Comment on the morphology of the erythrocytes.
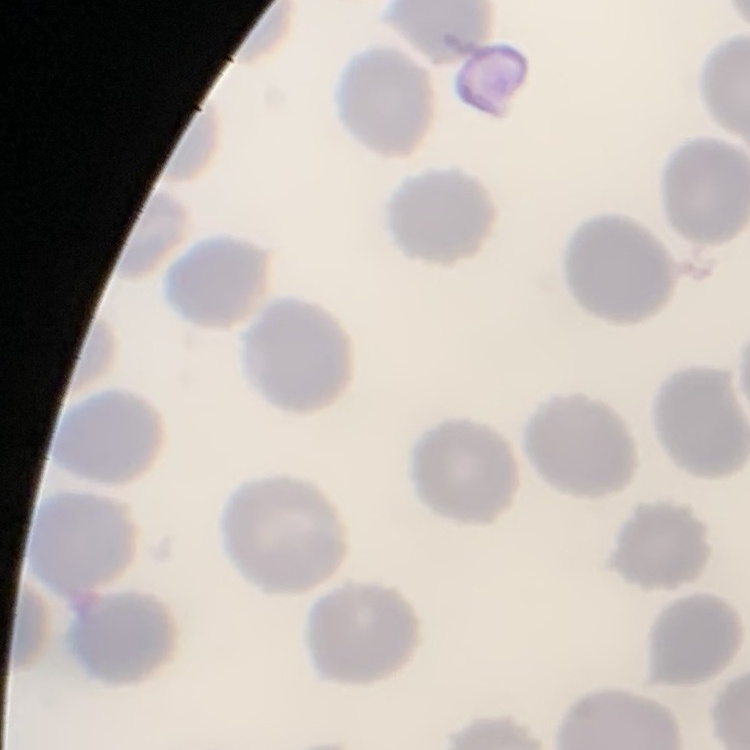

No rouleaux formation.

Stained with either Field's or Giemsa. Thin peripheral smear. One tile cut from a larger photomicrograph.